Name the parasite shown.
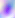

This is Toxoplasma gondii.

{
  "modality": "micrograph",
  "magnification": "400x"
}